Report the malaria status of this cell.
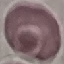
It is uninfected.

Cell patch, automatically extracted from a larger field of view and resized to 64 × 64 pixels. Acquired by smartphone through the microscope eyepiece. Thin smear of blood. Giemsa stain.